Point out each Plasmodium parasite.
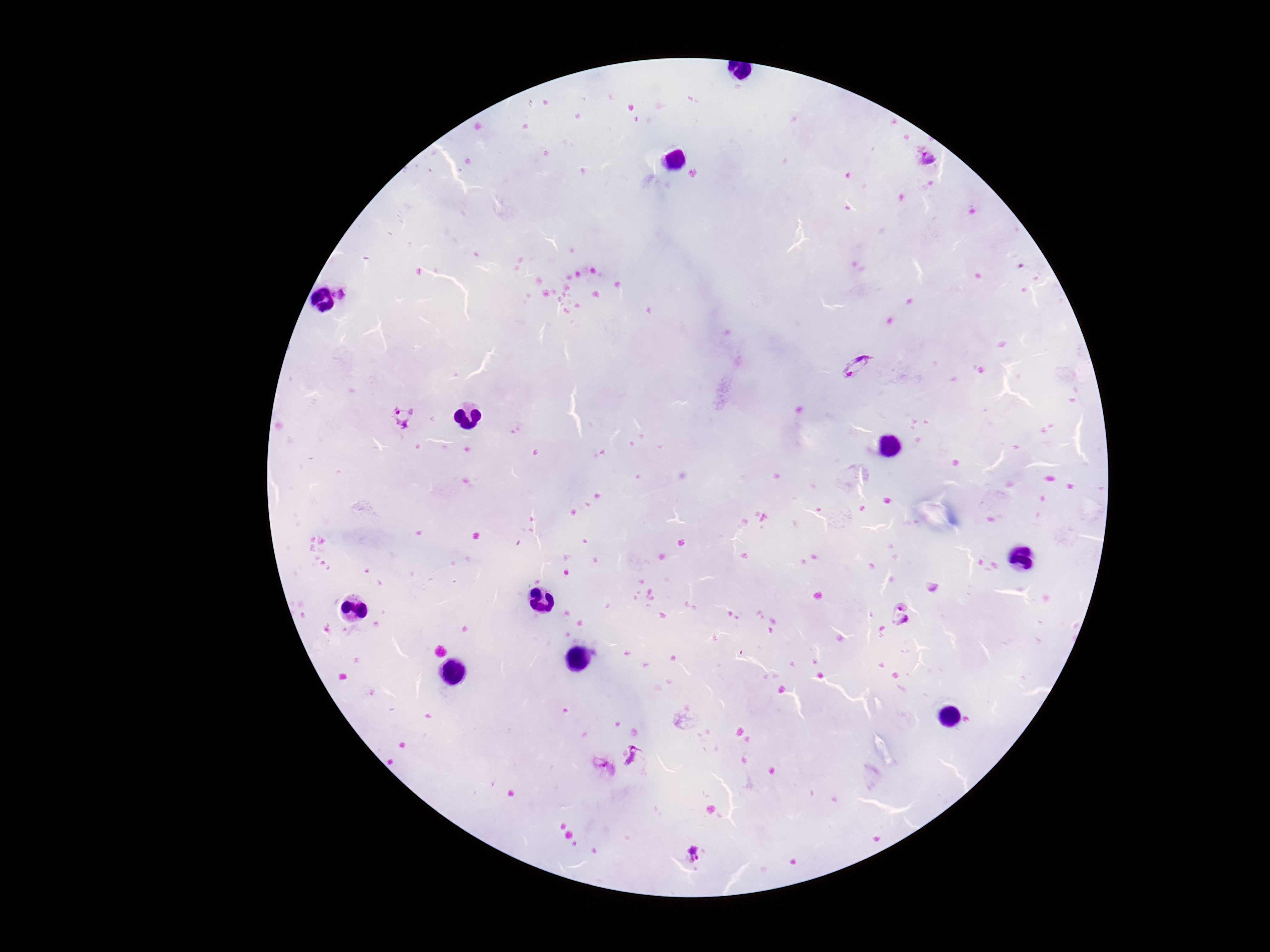

Approximate object centers, in pixels from the top-left corner.
Plasmodium parasites: (x=929, y=159), (x=344, y=292), (x=858, y=366), (x=401, y=417), (x=901, y=612), (x=635, y=759), (x=601, y=773), (x=695, y=856).

Summary:
  - Image size: 1270×952 pixels
  - Patient malaria status: infected
  - Magnification: 100x
  - Stain: Giemsa
  - Field of view: single
  - Capture: smartphone camera through the microscope eyepiece
  - Preparation: thick blood smear